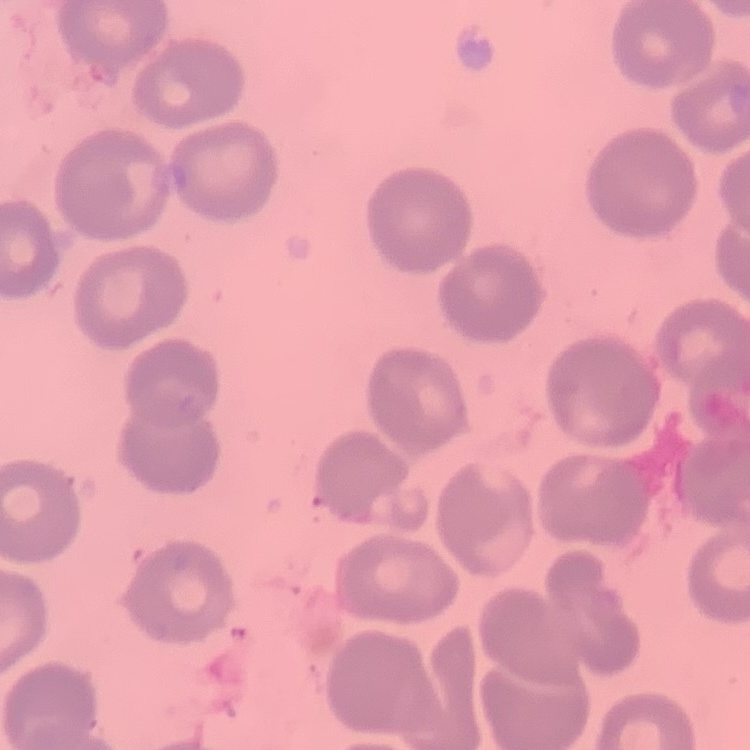 The red blood cells exhibit no rouleaux formation. Stained with either Field's or Giemsa. Thin blood smear. One tile cut from a larger photomicrograph.